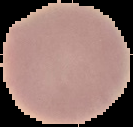

Summary:
  - Malaria status: uninfected
  - Preparation: thin blood film
  - Image size: 133×127 pixels
  - Image type: cell region segmented out of the field of view; surrounding area masked to black